Report the malaria status of this cell.
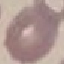
Uninfected.

Cell patch, automatically extracted from a larger field of view and resized to 64 × 64 pixels. Thin blood smear. Giemsa stain. Photographed with a smartphone camera at the microscope eyepiece.